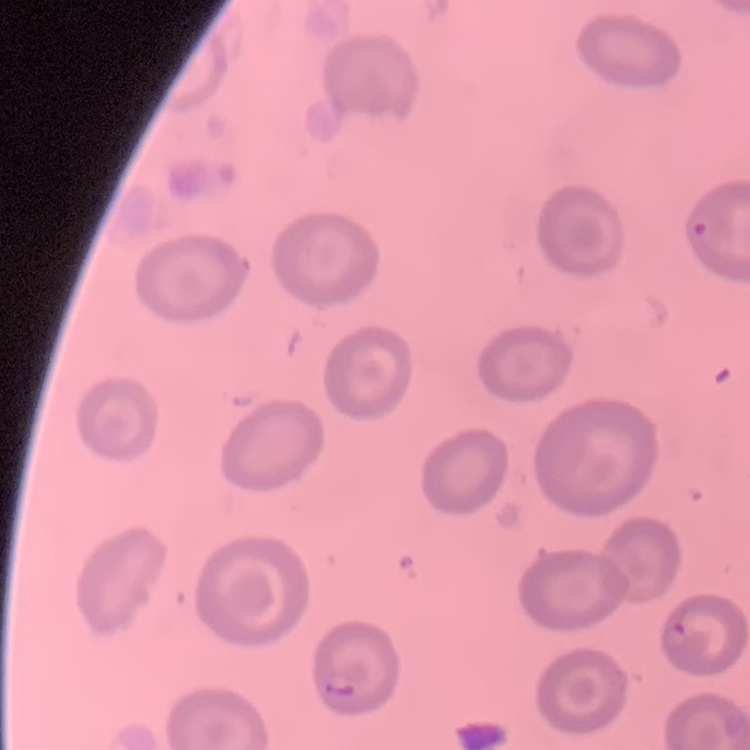
Summary:
  - Red blood cell morphology: no rouleaux formation
  - Stain: Field's or Giemsa
  - Preparation: thin blood smear
  - Image type: one tile cut from a larger photomicrograph